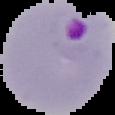
From a thin blood film. Cell region segmented out of the field of view; the surrounding area is masked to black. Malaria status: parasitized. Image is 115×115 pixels.